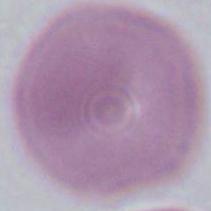
Summary:
  - Identification: red blood cell
  - Modality: photomicrograph
  - Magnification: 1000x